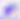

identification: Toxoplasma gondii
magnification: 400x
modality: photomicrograph